Locate every Plasmodium falciparum-infected red blood cell.
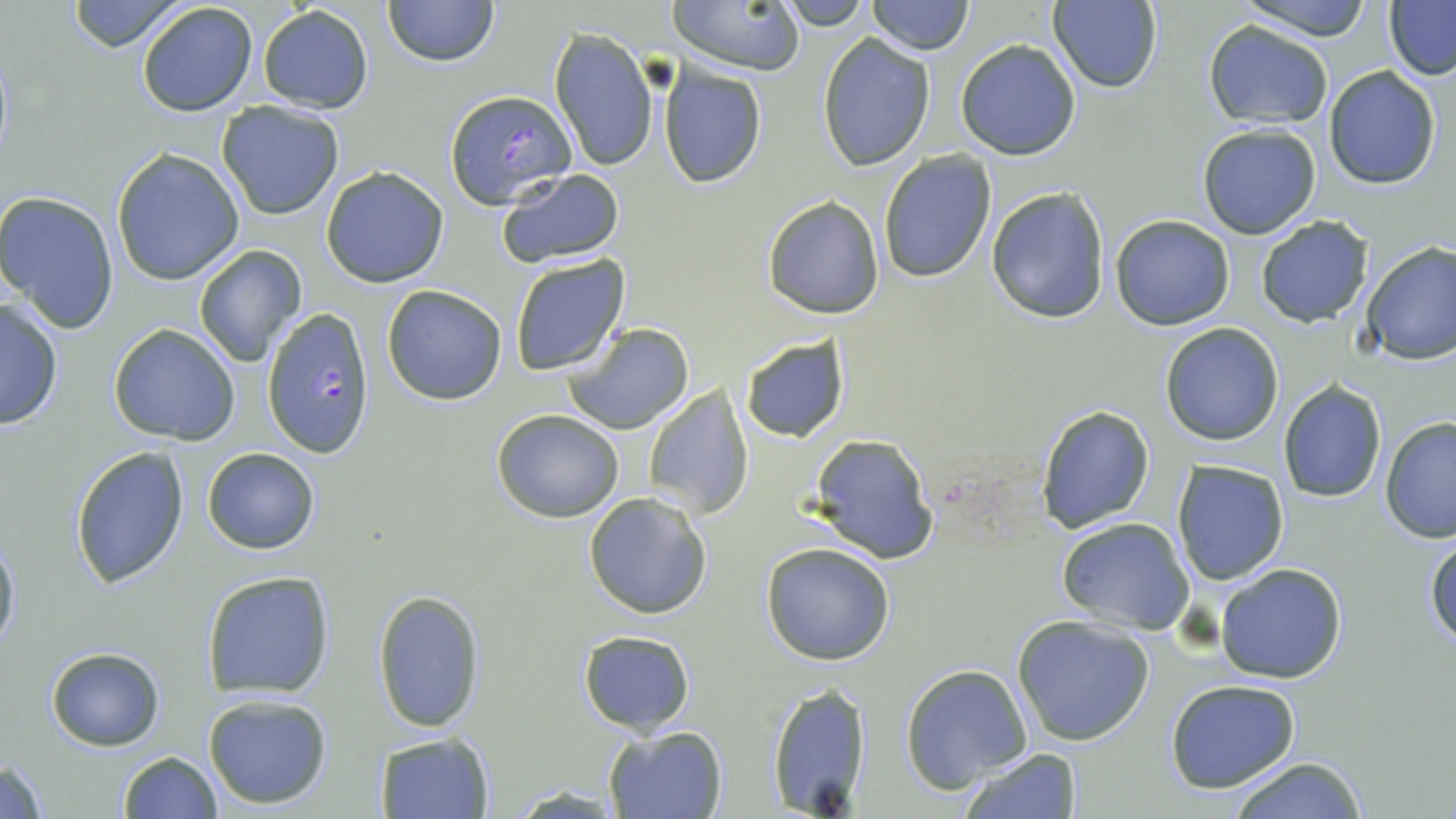
Approximate bounding boxes as [x1, y1, x2, y2] in pixels.
Plasmodium falciparum-infected red blood cells: [445, 89, 575, 209], [261, 309, 375, 457].

slide_level_diagnosis: Plasmodium falciparum
modality: light microscopy
stain: May-Grünwald-Giemsa
image_size: 1456×819 pixels
magnification: 1000x
field_of_view: single
preparation: thin blood film
uninfected_red_blood_cell_locations: 'approximate bounding boxes as [x1, y1, x2, y2] in pixels: [63, 0, 192, 52], [384, 0, 497, 67], [775, 0, 874, 30], [865, 0, 973, 55], [1049, 0, 1162, 93], [1233, 0, 1379, 40], [136, 1, 259, 117], [669, 1, 804, 75], [1385, 1, 1456, 80], [257, 6, 372, 114], [1202, 20, 1333, 129], [549, 28, 659, 172], [816, 32, 937, 171], [955, 39, 1081, 161], [660, 65, 767, 188], [1323, 65, 1441, 189], [217, 102, 345, 220], [1196, 124, 1323, 240], [111, 148, 244, 285], [877, 150, 997, 283], [321, 166, 448, 287], [494, 168, 625, 271], [985, 187, 1111, 325], [0, 190, 121, 332], [761, 195, 885, 319], [1110, 215, 1235, 331], [1255, 216, 1376, 328], [1265, 230, 1453, 353], [1359, 241, 1455, 367], [192, 245, 306, 365], [509, 255, 629, 375], [381, 284, 508, 404], [0, 299, 64, 429], [563, 322, 694, 435], [1160, 322, 1285, 446], [107, 324, 240, 445], [740, 336, 850, 444], [1278, 382, 1386, 503], [644, 387, 754, 517], [1035, 404, 1155, 533], [492, 408, 625, 522], [1379, 417, 1456, 543], [806, 434, 939, 564], [71, 445, 191, 590], [202, 447, 320, 554], [1172, 460, 1289, 586], [583, 491, 714, 619], [1056, 517, 1195, 636], [1, 530, 20, 657], [1425, 537, 1456, 650], [761, 542, 895, 665], [1214, 563, 1347, 682], [200, 569, 336, 700], [374, 588, 485, 733], [1012, 615, 1154, 746], [579, 630, 696, 734], [45, 646, 165, 750], [901, 664, 1033, 793], [1164, 679, 1301, 792], [765, 682, 872, 816], [203, 692, 334, 808], [603, 726, 728, 818], [383, 732, 498, 819], [960, 748, 1081, 819], [118, 749, 221, 818], [1226, 757, 1373, 818], [0, 758, 51, 817]'